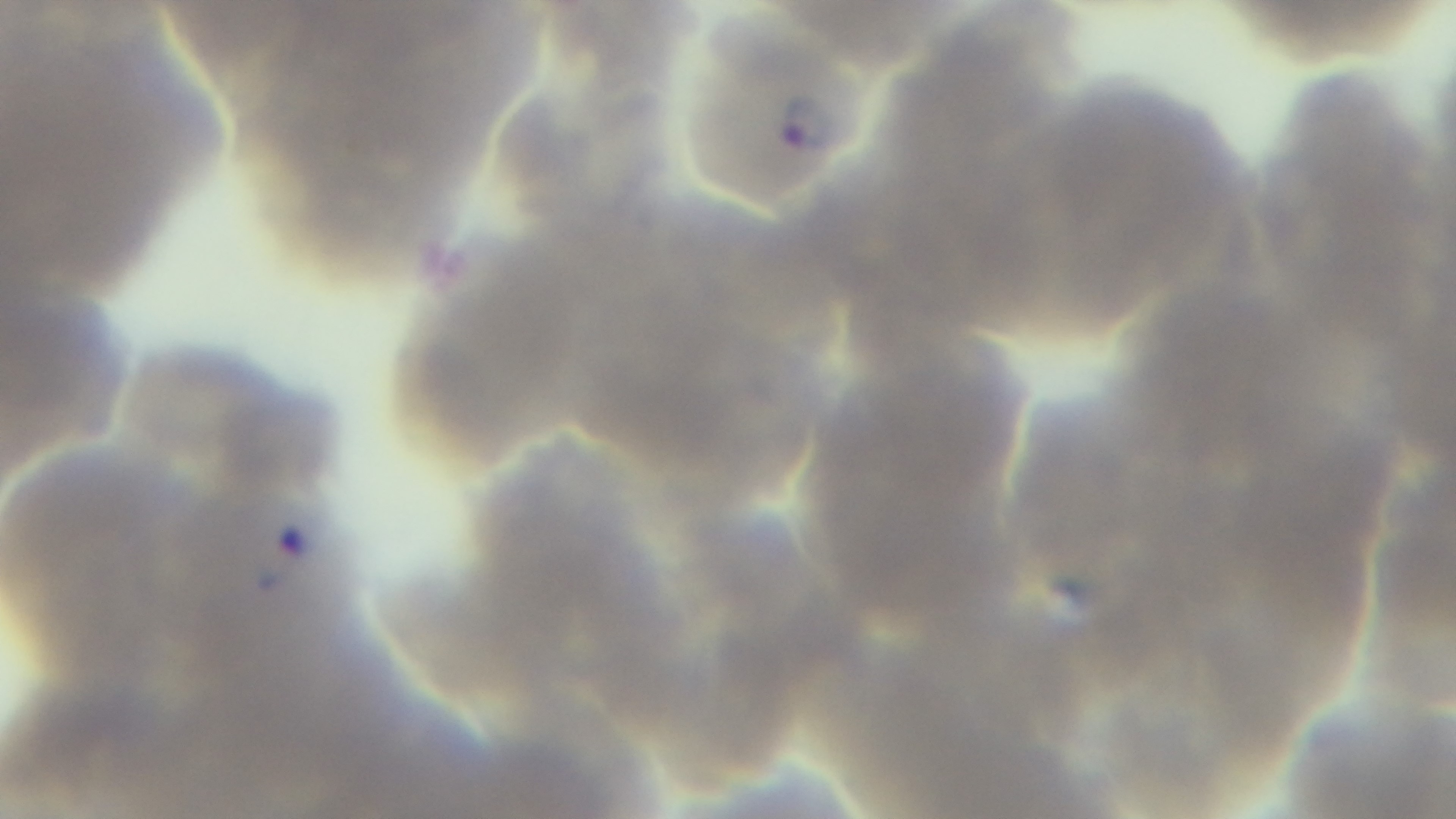 Malaria status: infected. Oil-immersion objective, 100x. One field from the slide. Photomicrograph. Captured with a mounted 4K digital camera. Giemsa stain. Preparation: thin.